Draw a bounding box around every parasitised red blood cell.
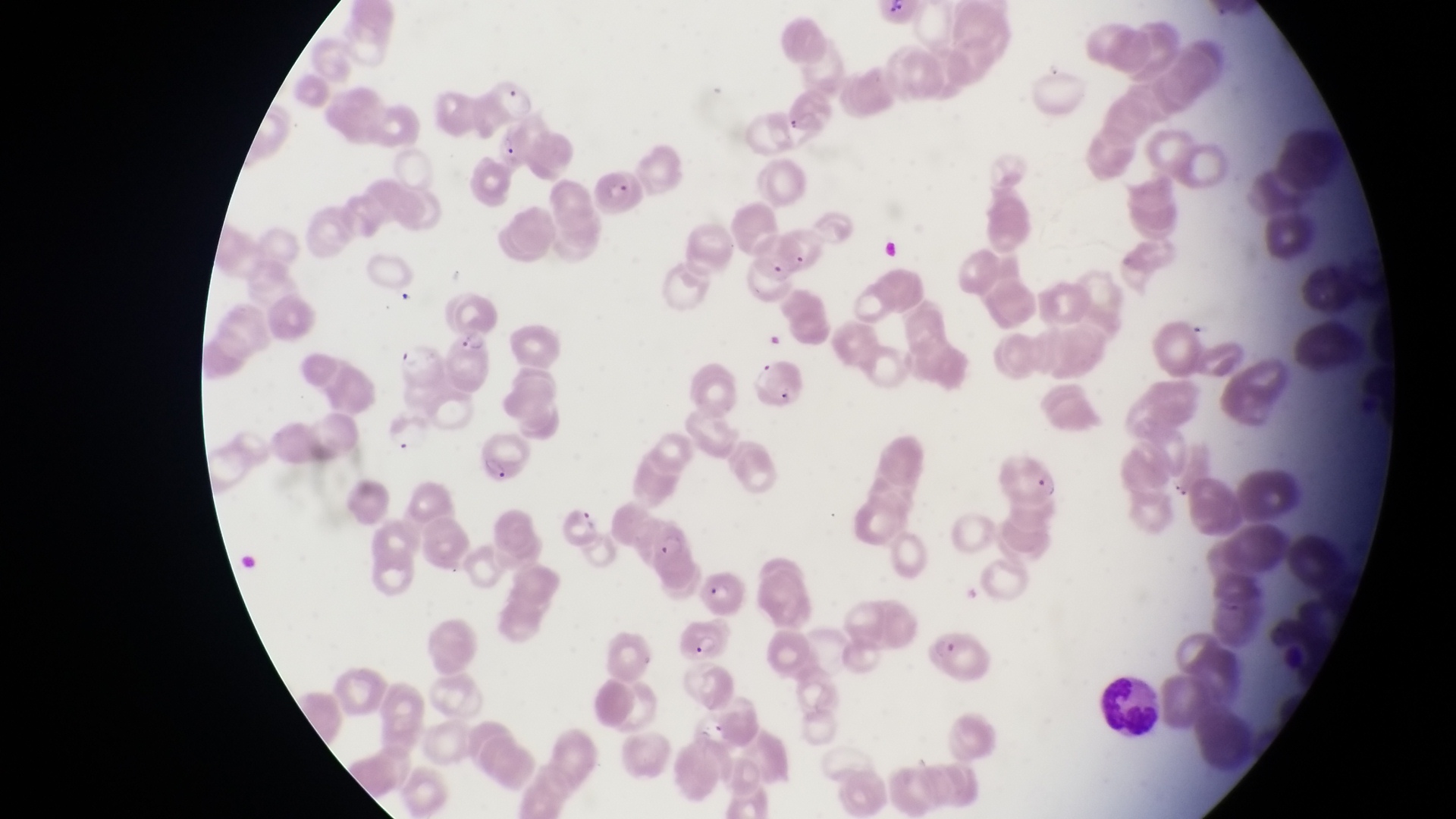
Approximate bounding boxes as (left, top, right, bottom) in pixels.
Parasitised red blood cells: (495, 133, 537, 176), (595, 165, 648, 221), (748, 230, 807, 280), (439, 330, 498, 391), (753, 363, 812, 416), (475, 441, 535, 486), (999, 450, 1063, 503), (558, 504, 601, 547), (642, 516, 697, 589), (695, 565, 747, 618), (668, 623, 729, 665), (928, 631, 991, 686).

{
  "leukocyte_locations": "approximate bounding boxes as (left, top, right, bottom) in pixels: (1089, 670, 1162, 739)",
  "preparation": "thin blood film",
  "magnification": "1000x",
  "capture": "smartphone photograph through the eyepiece of an Olympus CX-23 microscope",
  "image_size": "1456×819 pixels",
  "field_of_view": "single",
  "country": "Uganda",
  "trophozoite_locations": "approximate bounding boxes as (left, top, right, bottom) in pixels: (492, 79, 541, 128)"
}